Name the parasite shown.
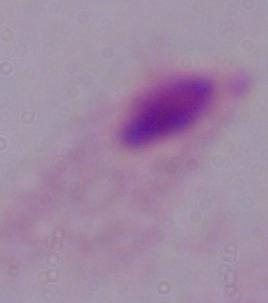

A trichomonad.

{
  "modality": "photomicrograph",
  "magnification": "1000x"
}